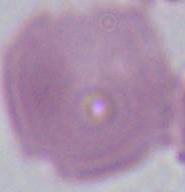
Summary:
  - Modality: micrograph
  - Magnification: 1000x
  - Identification: erythrocyte